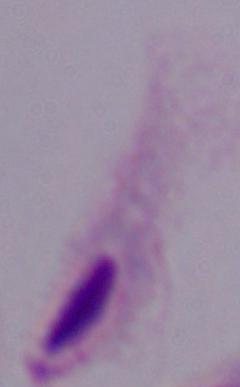 A trichomonad is shown. Photomicrograph. 1000x magnification.